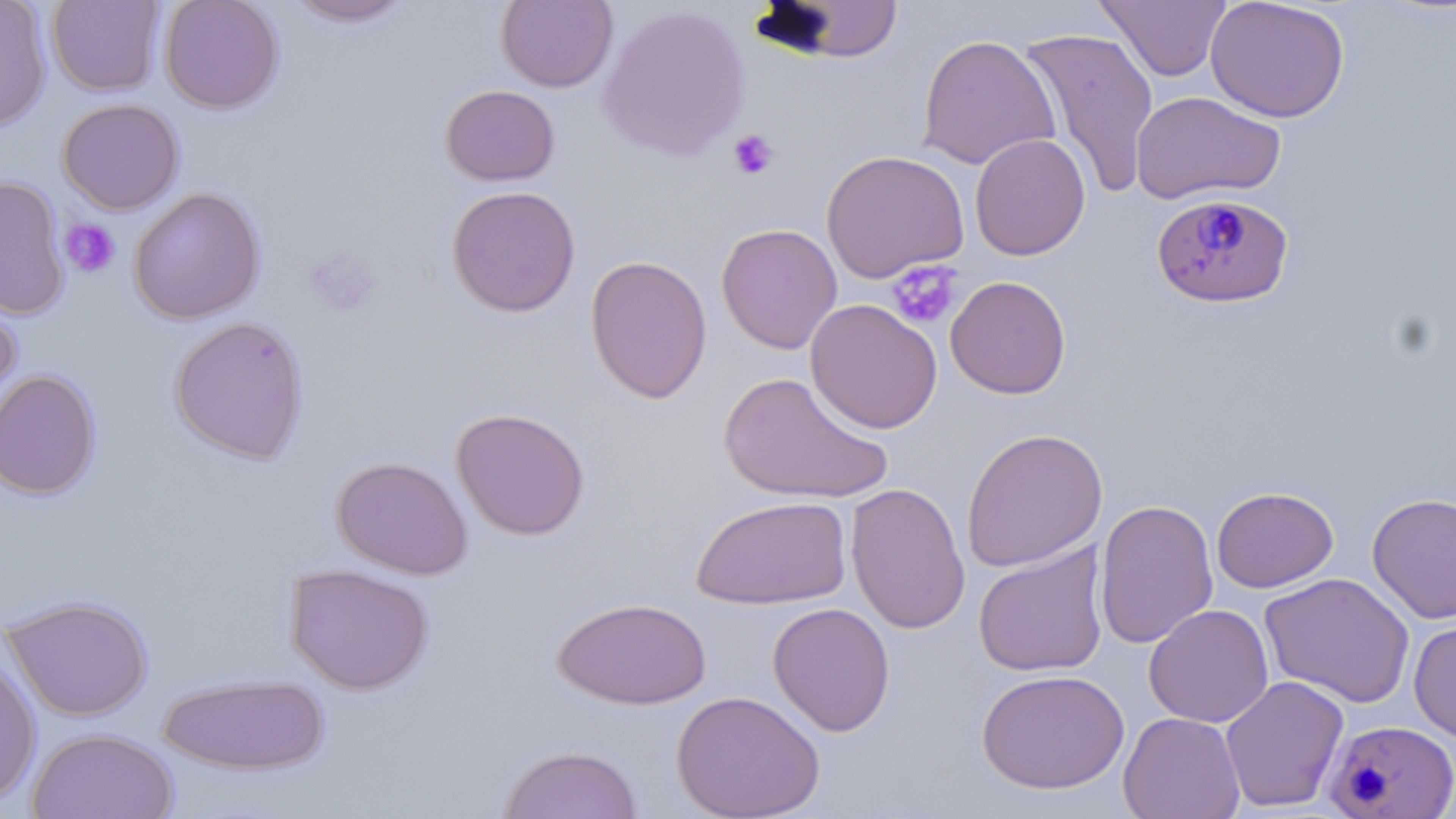

slide_level_diagnosis: Plasmodium falciparum
modality: optical microscopy
preparation: thin blood film
uninfected_red_blood_cell_locations: 'approximate bounding boxes as [x1, y1, x2, y2] in pixels: [46, 0, 164, 97], [159, 0, 284, 114], [287, 0, 414, 27], [1094, 0, 1232, 82], [1205, 0, 1350, 123], [0, 1, 52, 132], [496, 1, 618, 92], [752, 2, 907, 64], [597, 3, 751, 162], [1017, 26, 1160, 199], [917, 33, 1059, 171], [440, 84, 560, 186], [1130, 91, 1286, 205], [57, 98, 184, 215], [969, 133, 1091, 261], [821, 149, 970, 283], [0, 175, 70, 320], [445, 185, 581, 317], [128, 187, 266, 324], [715, 223, 843, 354], [585, 253, 714, 404], [945, 275, 1071, 399], [0, 283, 22, 424], [804, 299, 943, 434], [169, 315, 309, 465], [0, 368, 101, 500], [717, 371, 893, 505], [450, 407, 591, 540], [959, 427, 1109, 572], [331, 455, 473, 579], [844, 482, 971, 635], [1211, 486, 1338, 592], [1367, 492, 1456, 623], [690, 495, 852, 610], [1094, 498, 1219, 650], [972, 542, 1109, 678], [284, 563, 434, 695], [1259, 572, 1416, 708], [2, 595, 154, 721], [553, 596, 711, 710], [768, 602, 896, 736], [1144, 604, 1274, 728], [1408, 616, 1456, 744], [0, 648, 41, 807], [976, 668, 1129, 794], [156, 673, 330, 776], [1220, 675, 1349, 812], [671, 689, 826, 819], [1118, 711, 1246, 819], [27, 727, 178, 819], [496, 744, 643, 819]'
plasmodium_falciparum_infected_red_blood_cell_locations: 'approximate bounding boxes as [x1, y1, x2, y2] in pixels: [1150, 192, 1294, 308], [1323, 719, 1456, 817]'
platelet_locations: 'approximate bounding boxes as [x1, y1, x2, y2] in pixels: [728, 129, 780, 181], [59, 218, 121, 278], [306, 249, 379, 317], [886, 260, 963, 330]'
stain: May-Grünwald-Giemsa
image_size: 1456×819 pixels
field_of_view: single
magnification: 1000x